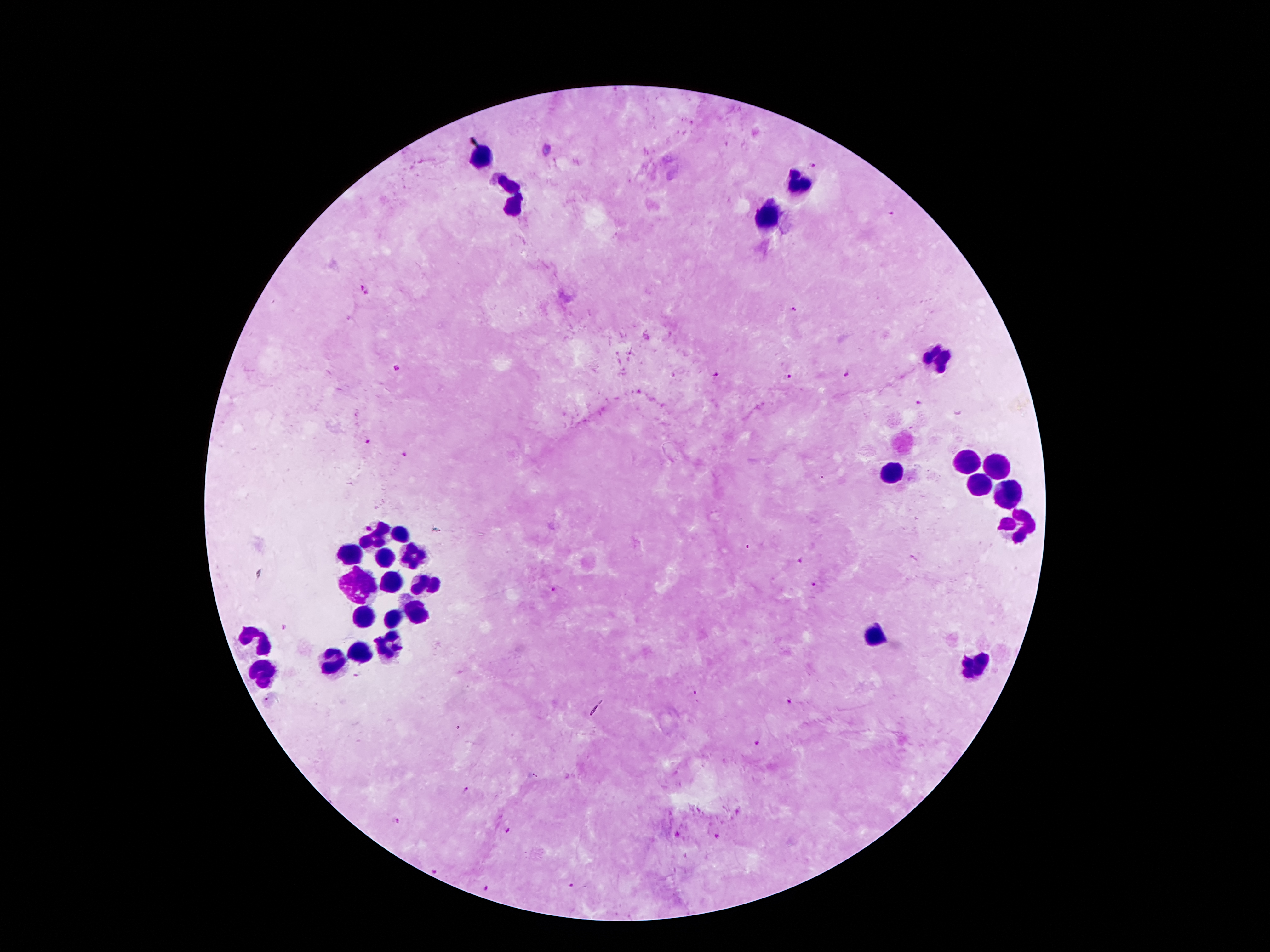

Approximate centers as {x, y} in pixels. Plasmodium parasite locations: {814, 163}, {892, 215}, {361, 287}, {367, 293}, {795, 309}, {396, 368}, {844, 373}, {715, 374}, {788, 376}, {918, 402}, {366, 441}, {404, 454}, {799, 559}, {813, 586}, {554, 589}, {790, 701}, {759, 743}, {465, 791}, {399, 821}, {510, 831}, {717, 836}, {433, 872}, {572, 886}, {486, 890}. Leukocyte locations: {484, 153}, {797, 183}, {514, 197}, {770, 216}, {938, 357}, {965, 461}, {995, 468}, {890, 475}, {978, 484}, {1009, 490}, {1020, 525}, {400, 536}, {377, 538}, {350, 553}, {413, 555}, {386, 557}, {361, 578}, {388, 582}, {424, 584}, {366, 615}, {417, 615}, {397, 618}, {871, 634}, {262, 641}, {382, 645}, {359, 653}, {336, 664}, {970, 666}, {264, 673}. Photographed through the microscope eyepiece with a smartphone camera. One field from this slide. Giemsa stain. Thick blood smear. Patient malaria status: infected with Plasmodium falciparum. Image is 1270×952 pixels. 100x magnification.